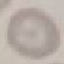
Summary:
  - Malaria status: uninfected
  - Stain: Giemsa
  - Capture: smartphone camera at the microscope eyepiece
  - Image type: automatically extracted cell patch, resized to 64 × 64 pixels
  - Preparation: thin blood film